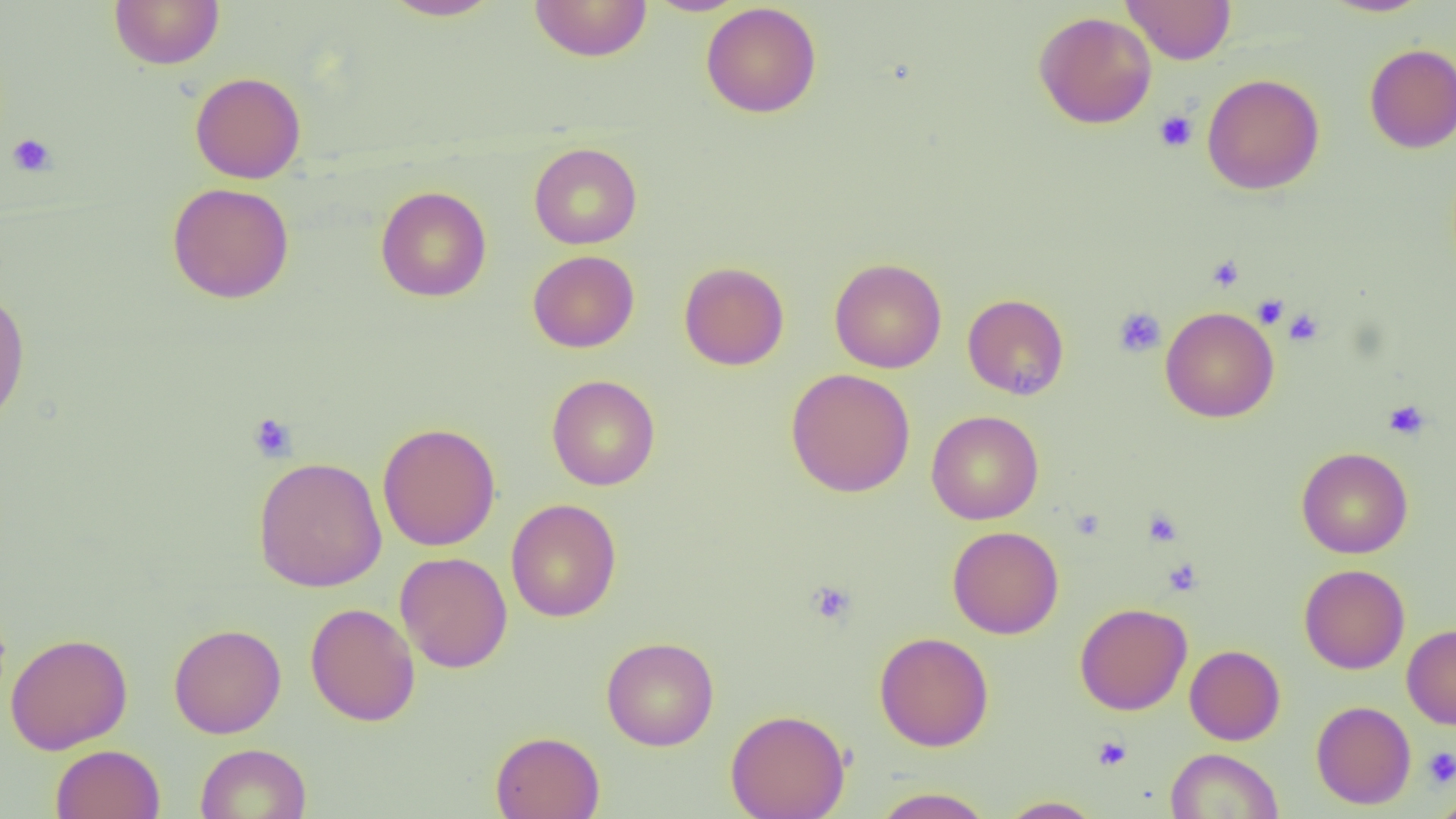
{
  "slide_level_diagnosis": "no evidence of blood parasites",
  "image_size": "1456×819 pixels",
  "platelet_locations": "approximate bounding boxes as named x1/y1/x2/y2 corners in pixels: (x1=1154, y1=110, x2=1198, y2=152), (x1=7, y1=133, x2=56, y2=177), (x1=1207, y1=255, x2=1245, y2=292), (x1=1252, y1=294, x2=1289, y2=328), (x1=1113, y1=307, x2=1166, y2=358), (x1=1283, y1=308, x2=1324, y2=346), (x1=1384, y1=400, x2=1430, y2=440), (x1=248, y1=412, x2=298, y2=462), (x1=1143, y1=509, x2=1183, y2=547), (x1=1163, y1=558, x2=1202, y2=596), (x1=807, y1=580, x2=856, y2=625), (x1=1093, y1=736, x2=1132, y2=771), (x1=1423, y1=746, x2=1456, y2=788)",
  "modality": "optical microscopy",
  "uninfected_red_blood_cell_locations": "approximate bounding boxes as named x1/y1/x2/y2 corners in pixels: (x1=109, y1=0, x2=225, y2=69), (x1=381, y1=0, x2=503, y2=21), (x1=644, y1=0, x2=748, y2=16), (x1=1121, y1=0, x2=1237, y2=65), (x1=1320, y1=0, x2=1433, y2=17), (x1=529, y1=1, x2=652, y2=62), (x1=701, y1=2, x2=822, y2=118), (x1=1033, y1=11, x2=1157, y2=129), (x1=1364, y1=43, x2=1456, y2=153), (x1=190, y1=71, x2=306, y2=184), (x1=1202, y1=73, x2=1325, y2=195), (x1=529, y1=142, x2=642, y2=249), (x1=167, y1=183, x2=295, y2=303), (x1=376, y1=186, x2=492, y2=302), (x1=528, y1=250, x2=640, y2=352), (x1=830, y1=258, x2=947, y2=373), (x1=678, y1=261, x2=789, y2=370), (x1=0, y1=287, x2=30, y2=430), (x1=962, y1=293, x2=1069, y2=400), (x1=1160, y1=305, x2=1279, y2=423), (x1=786, y1=368, x2=916, y2=497), (x1=546, y1=374, x2=660, y2=490), (x1=926, y1=410, x2=1044, y2=525), (x1=377, y1=422, x2=501, y2=551), (x1=1297, y1=447, x2=1413, y2=559), (x1=252, y1=456, x2=388, y2=592), (x1=505, y1=498, x2=621, y2=622), (x1=947, y1=526, x2=1064, y2=639), (x1=395, y1=552, x2=513, y2=673), (x1=1299, y1=564, x2=1410, y2=674), (x1=305, y1=602, x2=420, y2=726), (x1=1075, y1=602, x2=1192, y2=715), (x1=168, y1=623, x2=286, y2=738), (x1=1402, y1=623, x2=1456, y2=729), (x1=874, y1=631, x2=994, y2=752), (x1=4, y1=633, x2=133, y2=754), (x1=601, y1=636, x2=719, y2=751), (x1=1185, y1=644, x2=1285, y2=745), (x1=1311, y1=700, x2=1416, y2=809), (x1=725, y1=709, x2=851, y2=819), (x1=490, y1=730, x2=605, y2=819), (x1=195, y1=743, x2=311, y2=819), (x1=50, y1=744, x2=165, y2=818), (x1=1165, y1=748, x2=1284, y2=819), (x1=871, y1=787, x2=995, y2=818), (x1=1428, y1=794, x2=1456, y2=819), (x1=998, y1=796, x2=1105, y2=818)",
  "preparation": "thin blood smear",
  "magnification": "1000x",
  "field_of_view": "one of a larger specimen"
}